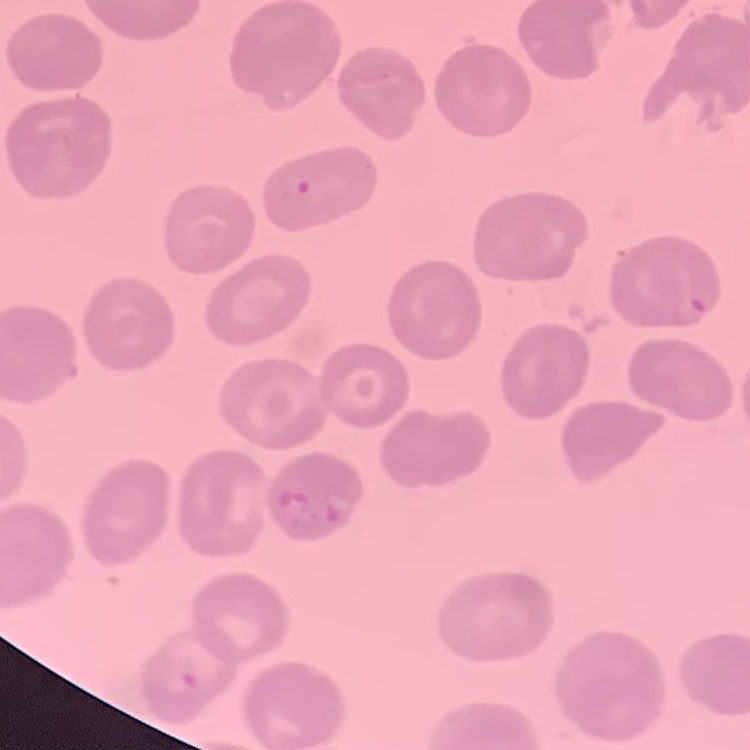

erythrocyte morphology = no rouleaux formation
preparation = thin blood smear
stain = Field's or Giemsa
image type = one tile cut from a larger photomicrograph